Describe the morphology of the red blood cells.
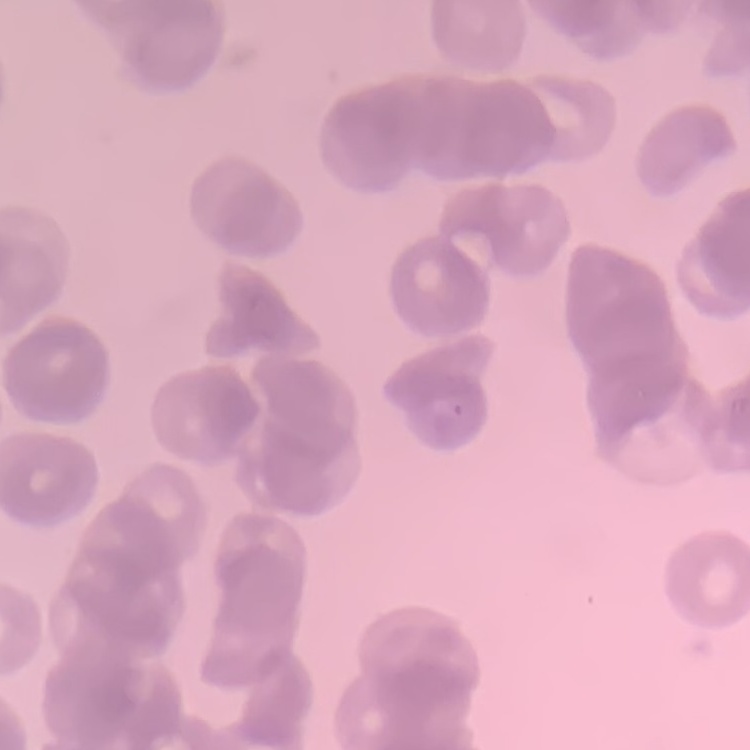

They show rouleaux formation.

{
  "image_type": "square crop of a larger photomicrograph",
  "stain": "Field's or Giemsa",
  "preparation": "thin blood film"
}